State which parasite is depicted.
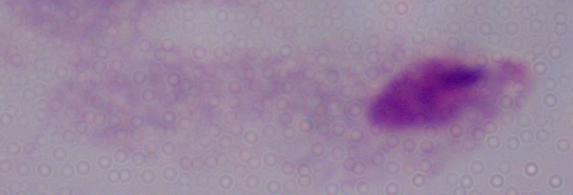

This is a trichomonad.

Summary:
  - Modality: micrograph
  - Magnification: 1000x